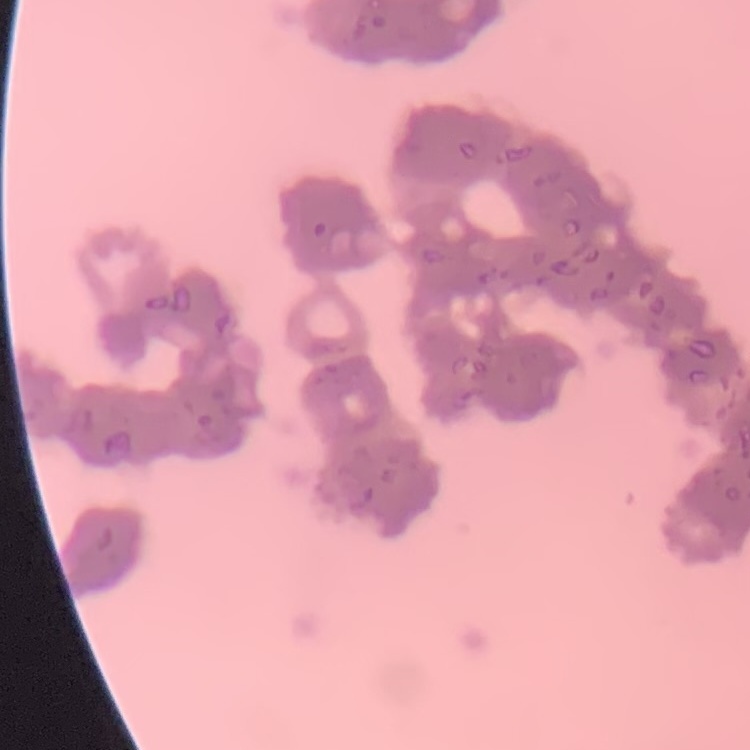

red blood cell morphology = rouleaux formation
preparation = thin peripheral smear
stain = Field's or Giemsa
image type = square crop of a larger photomicrograph